Locate every Plasmodium ovale-infected red blood cell.
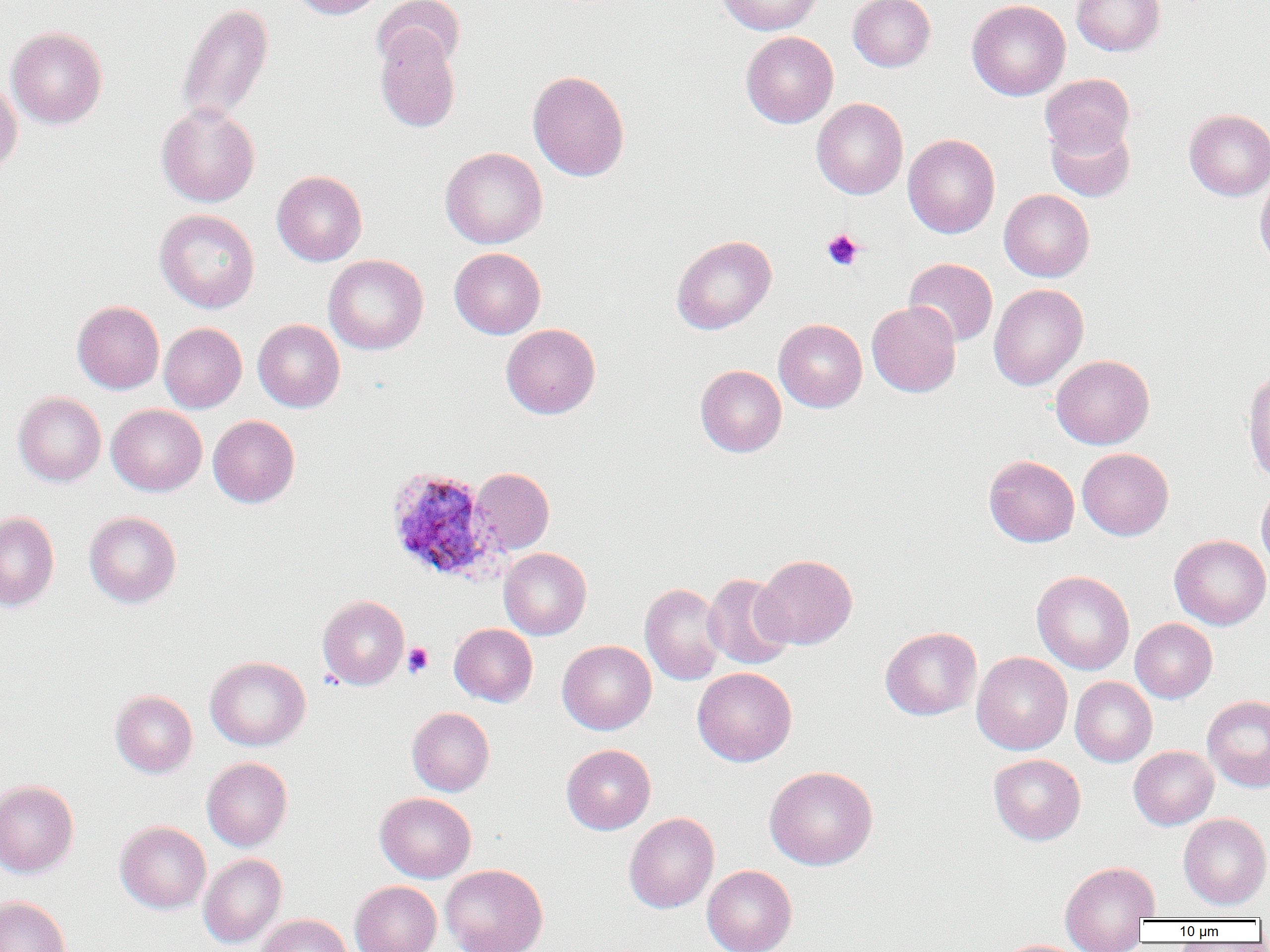
Approximate bounding boxes as (x1, y1, x2, y2) in pixels.
Plasmodium ovale-infected red blood cells: (384, 466, 499, 582).

Summary:
  - Platelet locations: (821, 229, 863, 271), (402, 642, 433, 678)
  - Uninfected red blood cell locations: (290, 0, 386, 19), (372, 0, 465, 73), (716, 0, 821, 35), (848, 0, 935, 72), (966, 0, 1071, 101), (1071, 0, 1165, 56), (176, 2, 274, 125), (374, 24, 461, 133), (6, 27, 108, 129), (741, 31, 838, 128), (527, 70, 630, 182), (1040, 73, 1135, 157), (0, 78, 23, 178), (811, 98, 908, 199), (156, 103, 260, 207), (1184, 109, 1270, 200), (1046, 120, 1135, 201), (903, 133, 1000, 238), (440, 146, 548, 249), (272, 171, 367, 266), (1254, 173, 1270, 269), (999, 189, 1095, 282), (155, 209, 260, 313), (671, 235, 776, 334), (449, 248, 546, 339), (323, 254, 428, 355), (904, 258, 998, 347), (989, 284, 1088, 390), (72, 300, 164, 394), (867, 301, 961, 397), (774, 318, 867, 412), (253, 319, 345, 412), (159, 322, 247, 413), (501, 324, 600, 419), (1051, 355, 1154, 449), (695, 365, 786, 457), (1242, 370, 1270, 483), (13, 392, 106, 486), (107, 404, 207, 496), (208, 415, 300, 508), (1077, 448, 1173, 540), (984, 455, 1079, 547), (470, 467, 554, 554), (1257, 484, 1270, 573), (84, 511, 182, 608), (0, 512, 59, 611), (1170, 535, 1270, 630), (499, 548, 591, 639), (753, 554, 857, 649), (1032, 570, 1134, 674), (702, 572, 794, 670), (640, 583, 726, 685), (317, 595, 409, 689), (1130, 618, 1217, 703), (449, 623, 537, 706), (880, 626, 982, 720), (557, 640, 656, 735), (972, 652, 1073, 755), (205, 656, 311, 751), (692, 667, 796, 766), (1070, 676, 1157, 766), (110, 689, 197, 778), (1202, 695, 1270, 792), (407, 707, 495, 796), (561, 744, 656, 834), (1129, 746, 1218, 830), (988, 754, 1086, 845), (202, 757, 293, 851), (764, 766, 878, 870), (0, 780, 79, 878), (375, 792, 476, 882), (624, 812, 719, 913), (1178, 813, 1270, 909), (115, 821, 211, 914), (199, 853, 287, 948), (1060, 860, 1159, 949), (440, 864, 548, 952), (702, 865, 797, 952), (350, 881, 441, 952), (0, 895, 72, 952), (255, 914, 353, 952), (996, 939, 1088, 952)
  - Slide-level diagnosis: Plasmodium ovale
  - Preparation: thin blood film
  - Magnification: 1000x
  - Image size: 1270×952 pixels
  - Modality: optical microscopy
  - Field of view: single